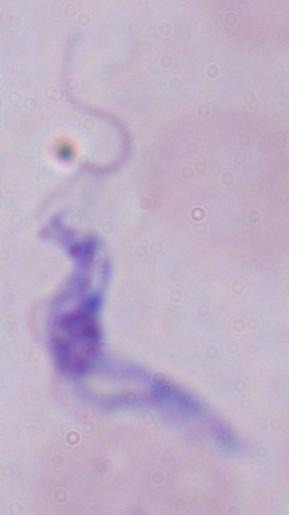 Photomicrograph. A trypanosome is seen. 1000x magnification.